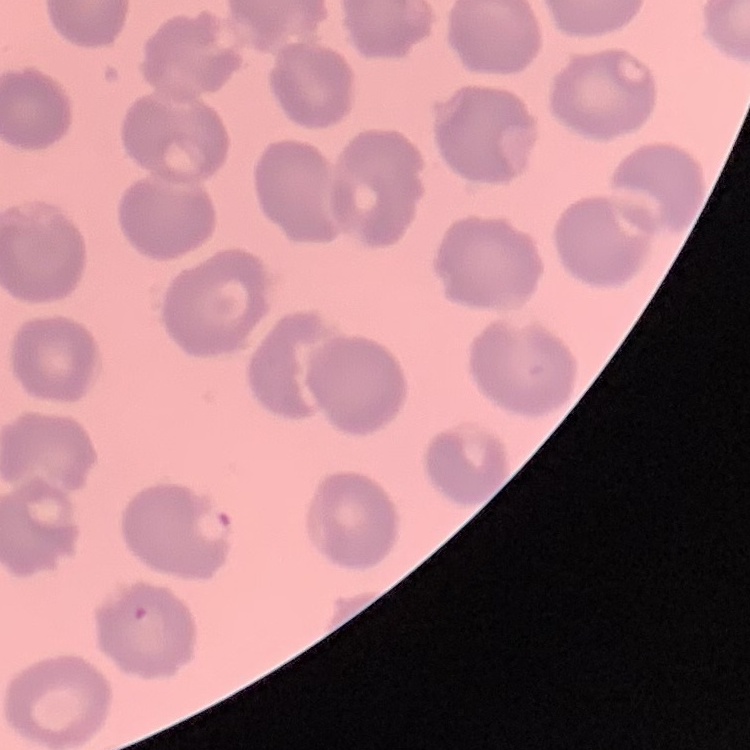

Summary:
  - Red blood cell morphology: no rouleaux formation
  - Preparation: thin peripheral smear
  - Stain: Field's or Giemsa
  - Image type: one tile cut from a larger photomicrograph